Assess this cell for malaria.
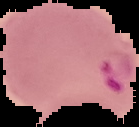

Parasitized.

image_type: segmented cell region with the area outside set to black
image_size: 139×127 pixels
preparation: thin blood smear